Assess for malaria.
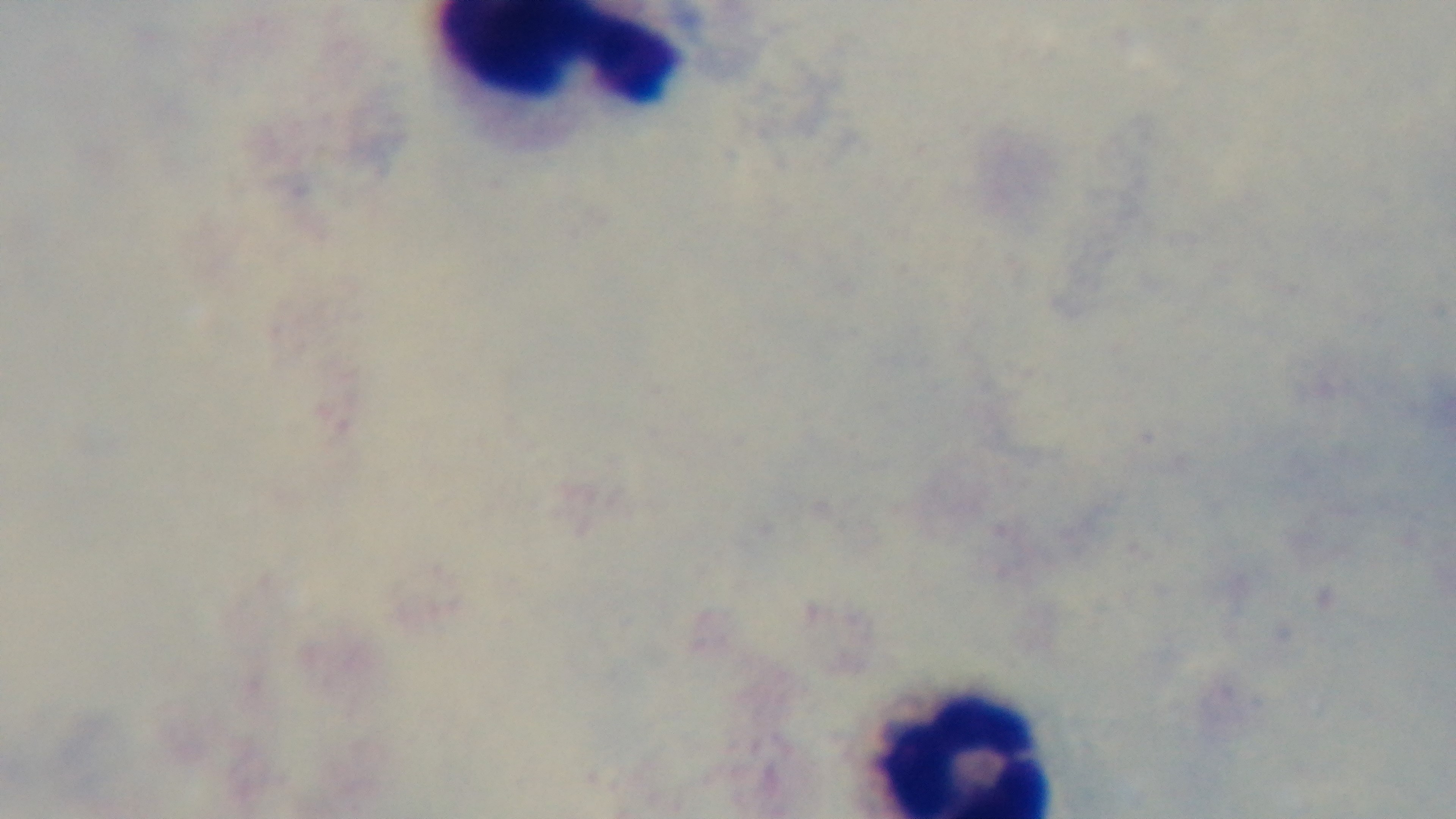

It is uninfected.

Light microscopy. Preparation: thick. Mounted 4K digital camera. One field from the slide. Giemsa-stained. Oil-immersion objective, 100x.